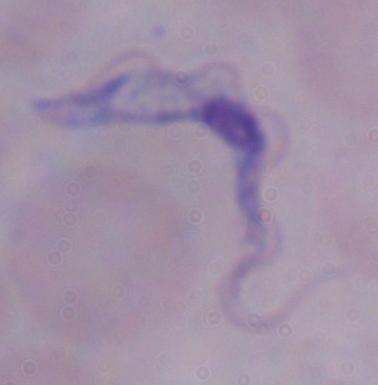

{
  "identification": "trypanosome",
  "modality": "photomicrograph",
  "magnification": "1000x"
}